Locate every leukocyte (white blood cell).
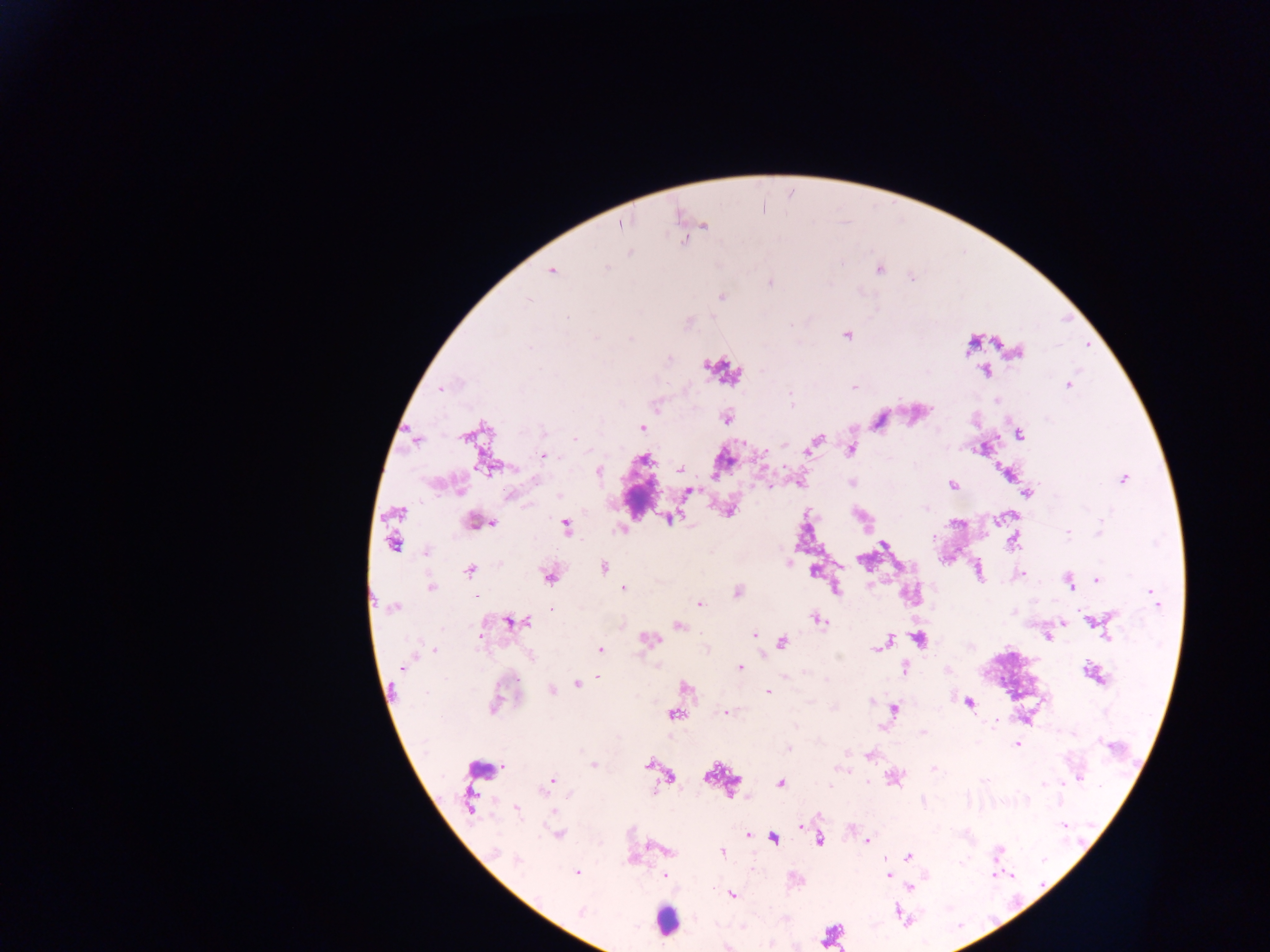

Approximate centers as x y in pixels.
Leukocytes: 721 370; 478 768; 665 919.

preparation: thick blood smear
country: Ghana
image_size: 1270×952 pixels
malaria_parasite_locations: 'approximate centers as x y in pixels: 620 224; 703 225; 878 269; 552 271; 771 283; 722 296; 846 334; 1016 351; 985 369; 1067 385; 854 386; 441 388; 996 400; 727 417; 879 421; 641 427; 1018 434; 416 438; 575 439; 815 441; 983 447; 850 448; 808 449; 542 455; 488 464; 680 470; 597 471; 1008 472; 1123 478; 852 482; 952 485; 687 491; 1027 493; 511 495; 729 510; 397 512; 670 518; 475 521; 565 526; 1013 539; 392 543; 884 545; 427 551; 861 560; 603 568; 469 570; 813 570; 549 574; 1017 574; 1097 579; 1070 582; 430 587; 623 587; 834 588; 737 592; 477 596; 698 603; 394 606; 551 609; 817 619; 1094 620; 513 621; 1061 621; 678 625; 754 635; 1048 636; 480 637; 918 638; 648 639; 885 641; 781 642; 879 646; 600 648; 740 668; 904 668; 1092 674; 598 677; 577 682; 685 687; 551 690; 767 692; 497 700; 968 702; 893 708; 727 712; 673 713; 1017 742; 787 748; 870 755; 649 764; 593 765; 934 768; 892 777; 669 778; 551 781; 781 783; 471 800; 516 808; 801 826; 558 833; 748 836; 773 837; 818 840; 867 840; 667 850; 721 851; 907 856; 631 860; 576 872; 664 875; 888 876; 910 887; 732 894; 580 911; 726 946'
field_of_view: single
capture: mobile-phone photograph through a microscope